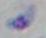
Micrograph. Captured at 1000x magnification. Toxoplasma gondii is shown.